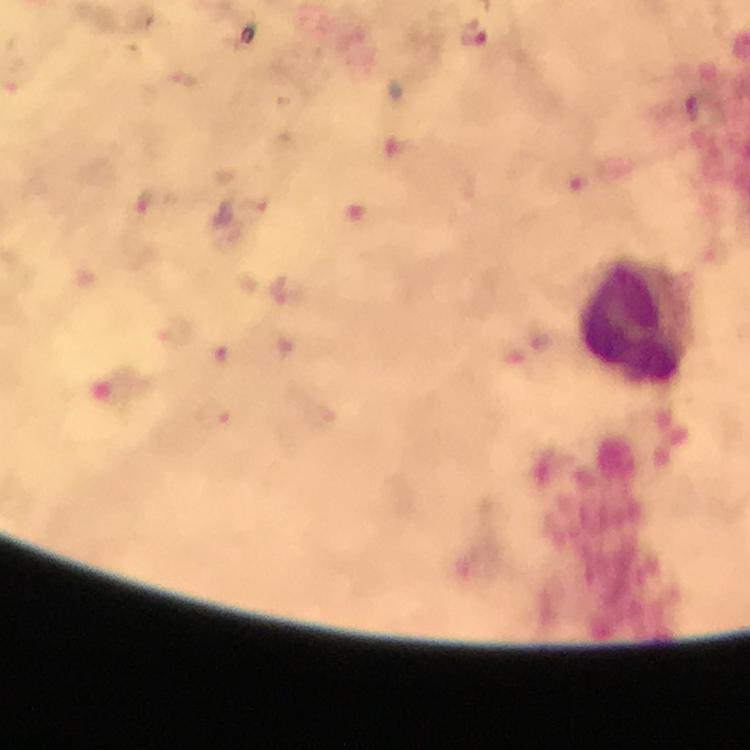
Approximate centers as (x, y) in pixels.
Summary:
  - Plasmodium parasite locations: (476, 35)
  - Leukocyte locations: (635, 326)
  - Magnification: 100x
  - Immersion oil: used
  - Capture: smartphone photograph through a microscope
  - Stain: Giemsa
  - Preparation: thick blood smear
  - Image size: 750×750 pixels
  - Context: from a malaria diagnostic workup
  - Cropped from: a single field of view